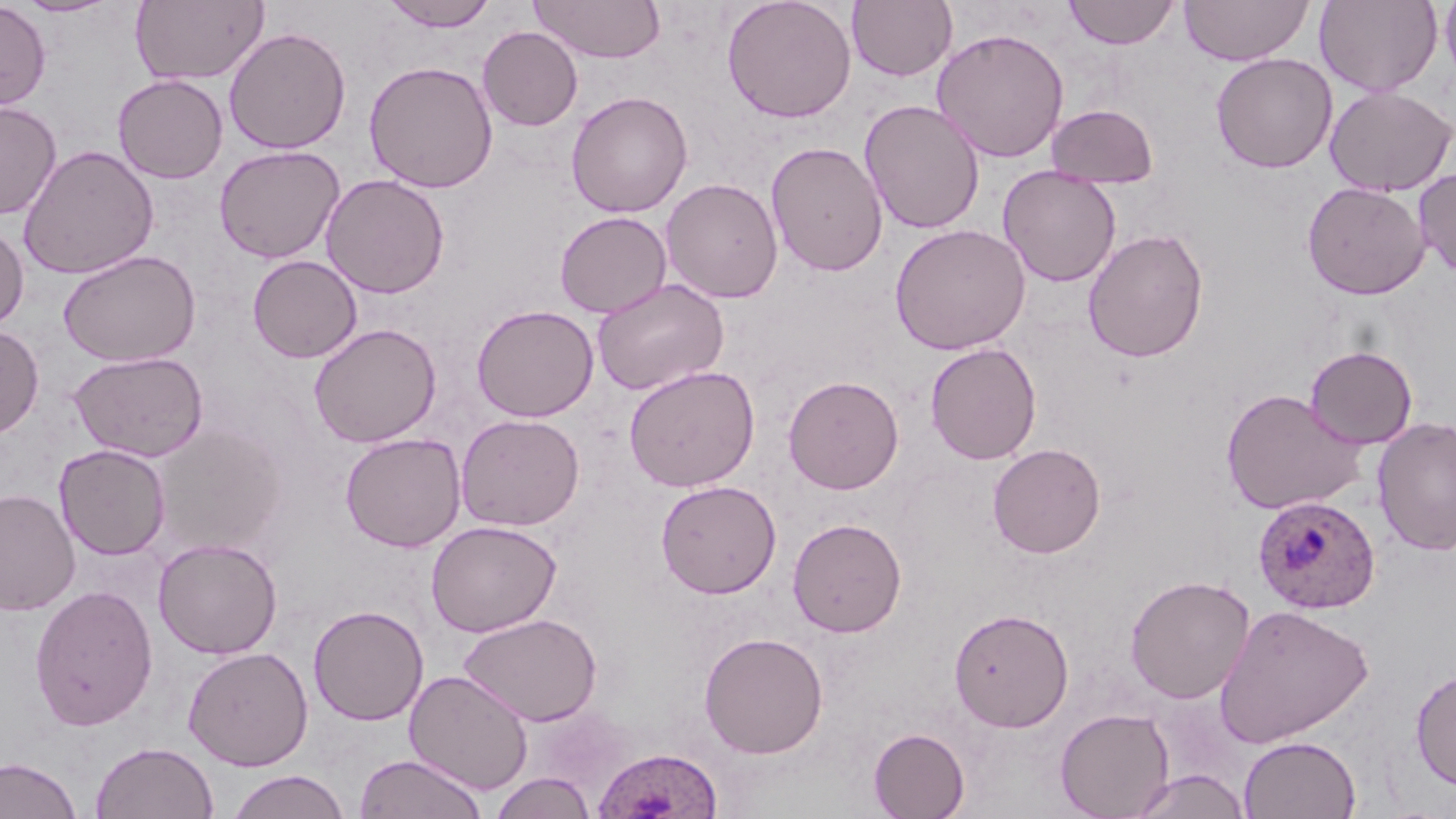
Approximate bounding boxes as (x1, y1, x2, y2) in pixels. Uninfected red blood cell locations: (13, 0, 120, 17), (130, 0, 269, 86), (381, 0, 498, 33), (530, 0, 666, 62), (721, 0, 857, 124), (847, 0, 957, 82), (1062, 0, 1181, 49), (1179, 0, 1313, 66), (1315, 0, 1442, 97), (1439, 0, 1456, 86), (0, 1, 51, 110), (224, 26, 351, 155), (477, 26, 583, 131), (931, 28, 1070, 163), (1210, 52, 1338, 173), (363, 60, 498, 193), (112, 74, 228, 183), (1324, 86, 1456, 197), (566, 91, 693, 218), (859, 99, 985, 235), (0, 101, 62, 220), (1045, 103, 1159, 188), (766, 141, 888, 277), (214, 144, 345, 263), (18, 145, 159, 280), (998, 166, 1121, 287), (1414, 166, 1456, 277), (320, 173, 450, 299), (661, 178, 784, 303), (1302, 181, 1430, 300), (554, 211, 671, 318), (0, 223, 29, 331), (889, 223, 1030, 355), (1083, 228, 1209, 363), (58, 249, 201, 367), (247, 255, 362, 363), (592, 278, 729, 396), (470, 304, 599, 422), (308, 322, 442, 448), (0, 324, 44, 438), (925, 342, 1042, 465), (1305, 345, 1418, 449), (69, 351, 208, 462), (623, 365, 760, 491), (783, 375, 904, 494), (1220, 387, 1367, 516), (455, 413, 585, 531), (1372, 416, 1456, 556), (149, 424, 288, 558), (339, 432, 466, 552), (988, 442, 1106, 558), (54, 444, 171, 560), (655, 480, 782, 599), (0, 488, 81, 616), (787, 517, 907, 638), (425, 520, 562, 637), (153, 537, 283, 659), (1125, 574, 1255, 704), (29, 584, 159, 731), (1214, 603, 1374, 748), (308, 605, 429, 726), (949, 608, 1074, 732), (458, 612, 602, 726), (698, 631, 829, 759), (182, 645, 313, 770), (1410, 667, 1456, 792), (404, 669, 533, 795), (1055, 707, 1175, 819), (868, 727, 970, 818), (1238, 735, 1362, 818), (90, 742, 219, 819), (354, 753, 488, 819), (0, 756, 82, 819), (1129, 769, 1251, 819), (225, 770, 352, 819), (490, 772, 597, 819). Plasmodium ovale-infected red blood cell locations: (1252, 495, 1381, 615), (594, 750, 724, 819). Slide-level diagnosis: Plasmodium ovale. One field of a larger specimen. Image is 1456×819 pixels. Light microscopy. May-Grünwald-Giemsa-stained preparation. Captured at 1000x magnification. Thin blood smear.